Report the malaria status of this cell.
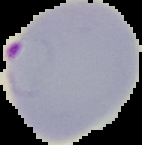
Parasitized.

The area outside the segmented cell region is set to black. From a thin blood smear. Image is 142×145 pixels.